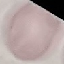 Malaria status: uninfected. Photographed with a smartphone camera at the microscope eyepiece. Automatically extracted cell patch, resized to 64 × 64 pixels. Thin smear of blood. Giemsa-stained preparation.